Comment on the morphology of the erythrocytes.
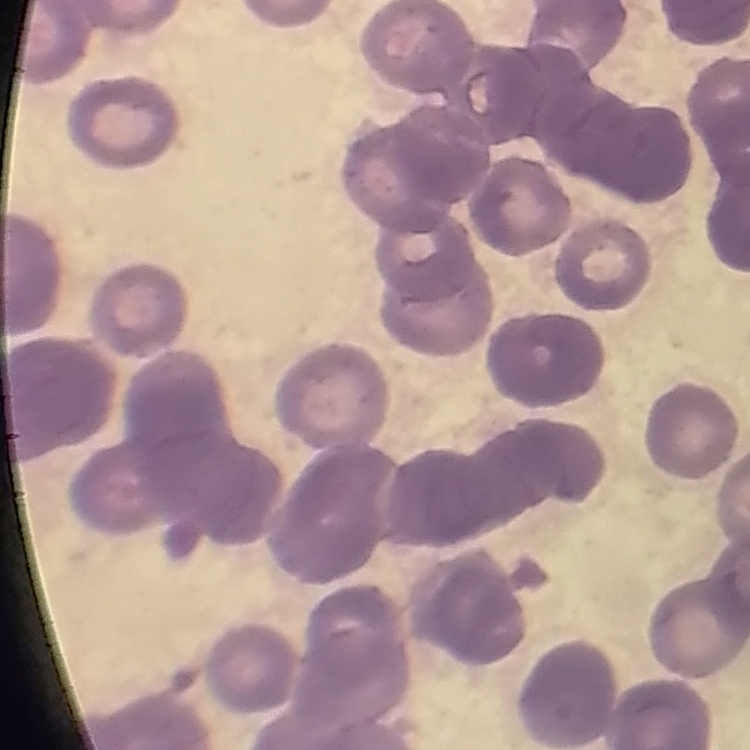
Rouleaux formation.

Thin blood film. Stained with either Field's or Giemsa. Square crop of a larger photomicrograph.